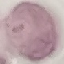
Summary:
  - Malaria status: uninfected
  - Image type: cell patch, automatically extracted from a larger field of view and resized to 64 × 64 pixels
  - Capture: smartphone camera at the microscope eyepiece
  - Stain: Giemsa
  - Preparation: thin blood smear